Assess the morphology of the erythrocytes.
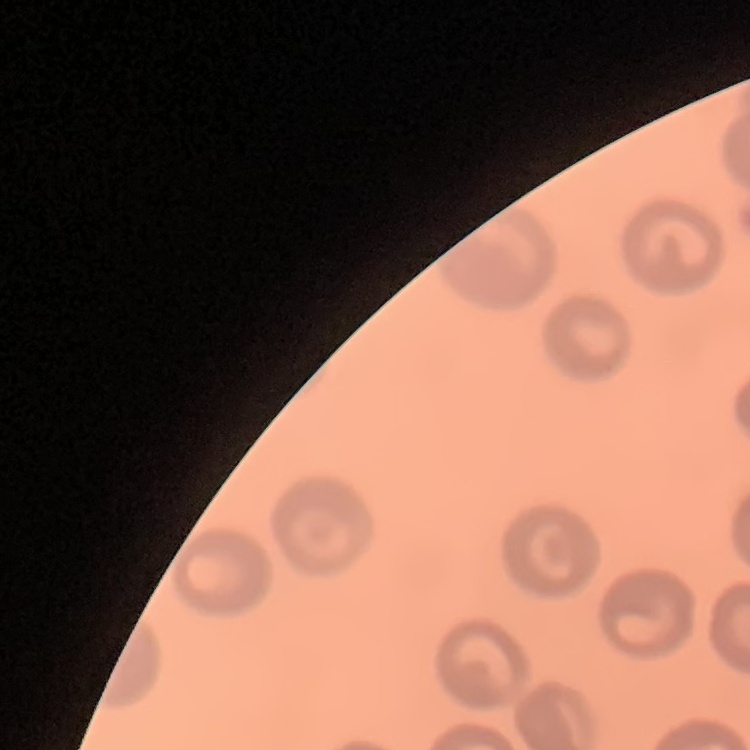

They show no rouleaux formation.

stain = Field's or Giemsa
image type = one tile cut from a larger photomicrograph
preparation = thin blood smear